Comment on the morphology of the erythrocytes.
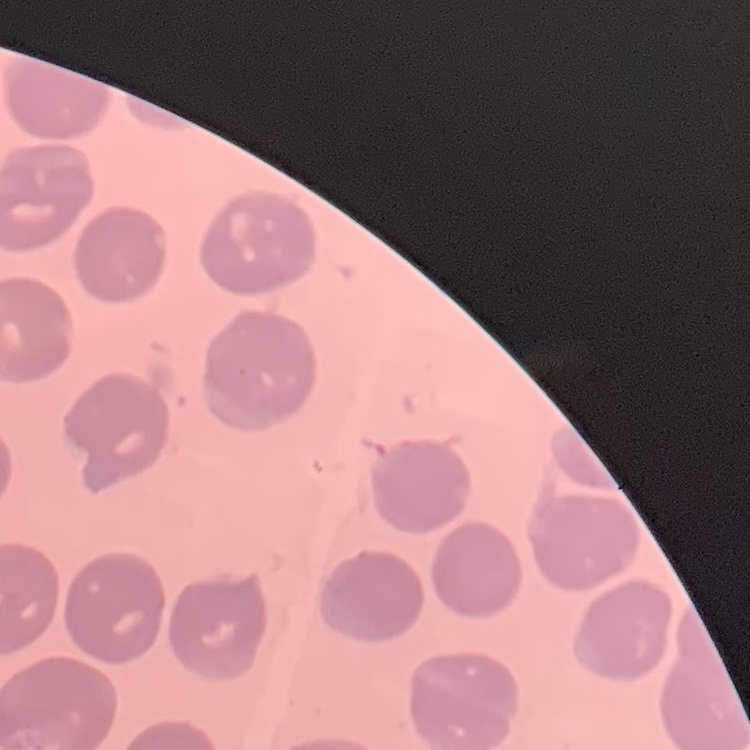

They show no rouleaux formation.

image type = square crop of a larger photomicrograph
stain = Field's or Giemsa
preparation = thin peripheral smear